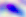 Captured at 400x magnification. Toxoplasma gondii is shown. Micrograph.